Assess the morphology of the erythrocytes.
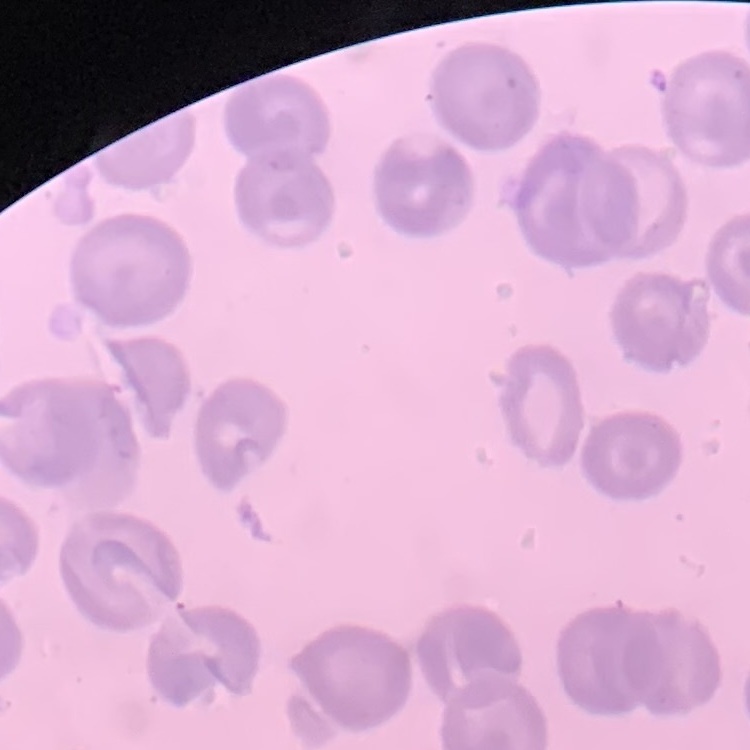
No rouleaux formation.

Summary:
  - Stain: Field's or Giemsa
  - Preparation: thin peripheral smear
  - Image type: square crop of a larger photomicrograph